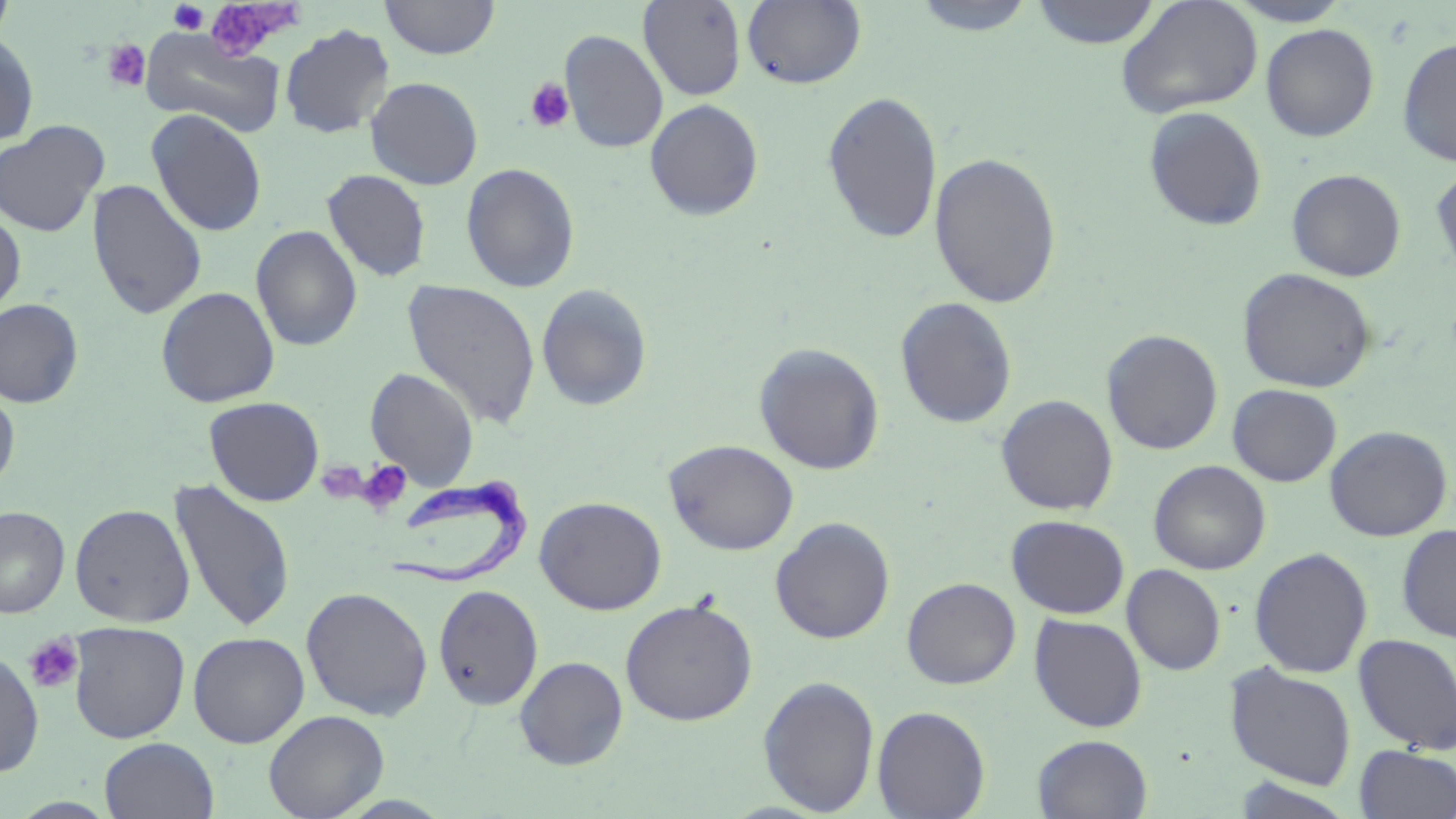
Approximate bounding boxes as (x1, y1, x2, y2) in pixels. Uninfected red blood cell locations: (380, 0, 500, 59), (638, 0, 747, 101), (910, 0, 1039, 36), (1030, 0, 1162, 49), (1115, 0, 1264, 119), (1224, 0, 1354, 26), (0, 1, 17, 49), (742, 1, 866, 90), (1261, 23, 1379, 142), (279, 24, 394, 139), (140, 28, 286, 138), (559, 30, 668, 153), (0, 31, 39, 147), (1397, 37, 1456, 167), (365, 77, 483, 189), (821, 90, 943, 244), (645, 99, 764, 220), (1143, 106, 1267, 232), (146, 109, 267, 237), (0, 120, 109, 238), (929, 151, 1063, 310), (461, 162, 580, 293), (1430, 162, 1456, 279), (1286, 168, 1407, 282), (322, 169, 432, 282), (87, 179, 207, 320), (0, 208, 26, 319), (251, 225, 362, 351), (1238, 268, 1376, 393), (402, 279, 541, 428), (536, 283, 653, 411), (156, 286, 280, 407), (894, 297, 1017, 428), (0, 298, 84, 408), (1101, 329, 1223, 454), (753, 342, 885, 475), (365, 367, 479, 489), (1227, 384, 1342, 487), (0, 387, 20, 493), (995, 394, 1118, 515), (204, 396, 324, 506), (1325, 425, 1452, 541), (664, 439, 799, 555), (1149, 460, 1271, 575), (168, 479, 296, 634), (534, 496, 667, 615), (69, 502, 195, 627), (0, 506, 70, 618), (1007, 515, 1130, 619), (770, 517, 895, 644), (1396, 524, 1456, 643), (1249, 547, 1373, 678), (1122, 564, 1226, 675), (902, 577, 1021, 689), (433, 584, 544, 711), (300, 586, 433, 720), (620, 597, 758, 726), (1028, 614, 1148, 732), (68, 622, 190, 743), (188, 631, 309, 748), (1353, 633, 1456, 755), (0, 647, 44, 777), (514, 656, 628, 769), (1224, 663, 1357, 790), (757, 674, 880, 816), (872, 706, 991, 819), (263, 709, 389, 819), (1032, 734, 1153, 818), (99, 737, 219, 819), (1354, 745, 1456, 819), (1232, 776, 1356, 819). Trypanosoma brucei locations: (378, 479, 533, 585). Platelet locations: (205, 1, 300, 65), (168, 2, 208, 34), (102, 39, 151, 92), (524, 76, 574, 132), (357, 459, 412, 514), (24, 634, 84, 694). Slide-level diagnosis: Trypanosoma brucei. Optical microscopy. 1000x magnification. May-Grünwald-Giemsa-stained preparation. Thin blood film. Single field of view. Image is 1456×819 pixels.